Give the position of every leukocyte visible.
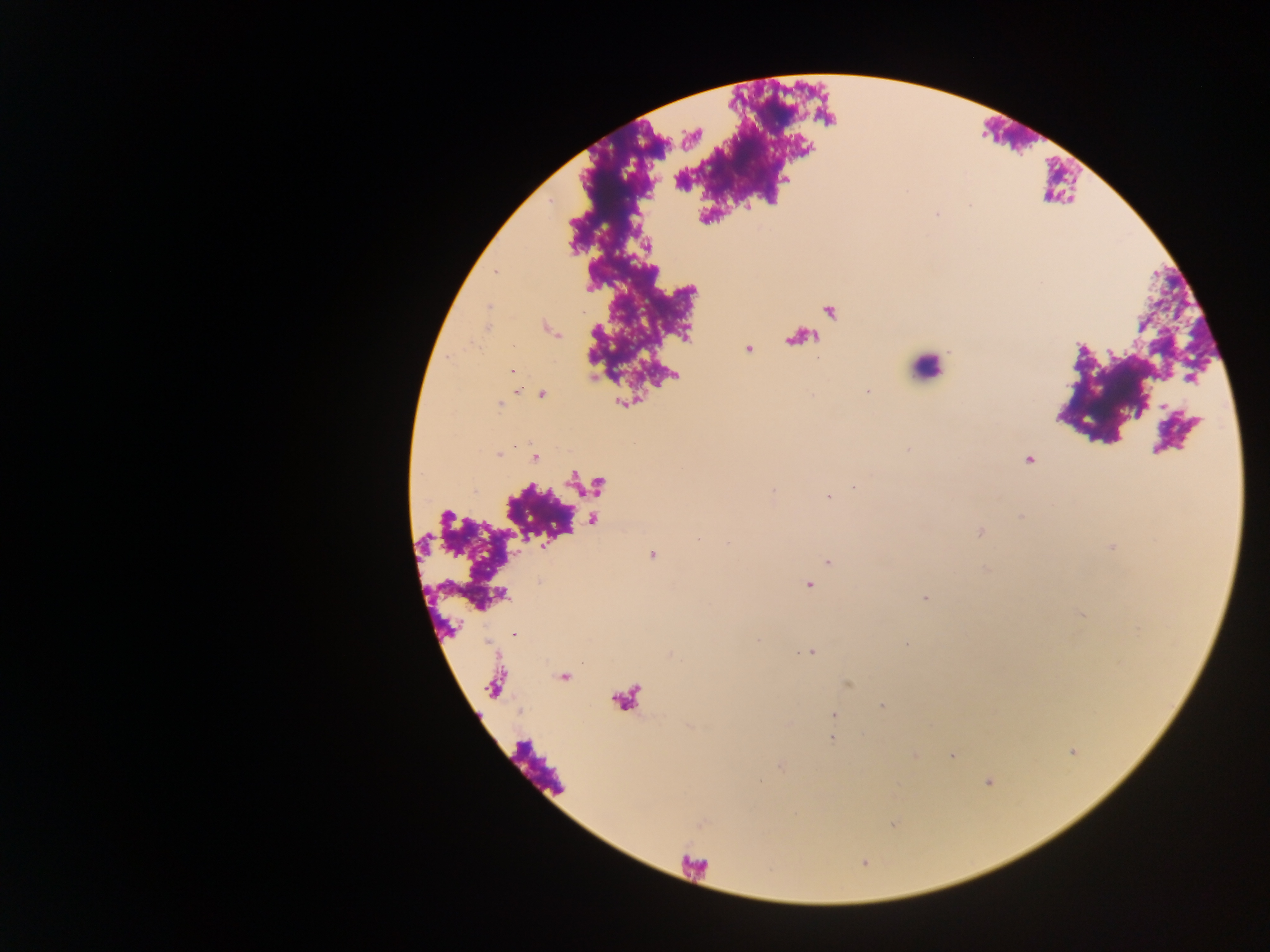

Approximate centers as {x, y} in pixels.
Leukocytes: {926, 366}.

capture: mobile-phone photograph through a microscope
image_size: 1270×952 pixels
field_of_view: single
country: Ghana
preparation: thick blood film
malaria_parasite_locations: 'approximate centers as {x, y} in pixels: {937, 215}, {867, 391}, {542, 395}, {1164, 406}, {907, 450}, {500, 454}, {536, 458}, {1028, 460}, {854, 486}, {773, 491}, {828, 497}, {1020, 516}, {979, 532}, {697, 539}, {728, 543}, {652, 555}, {827, 562}, {808, 585}, {925, 598}, {514, 635}, {907, 643}, {811, 652}, {882, 706}, {834, 715}, {832, 739}, {953, 755}, {759, 781}'